Classify this cell by malaria status.
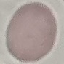
Uninfected.

capture = smartphone through the microscope eyepiece
stain = Giemsa
image type = automatically extracted cell patch, resized to 64 × 64 pixels
preparation = thin blood film